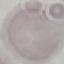

result = negative for malaria parasites
stain = Giemsa
preparation = thin blood film
image type = cell patch, automatically extracted from a larger field of view and resized to 64 × 64 pixels
capture = smartphone through the microscope eyepiece